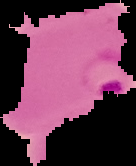
The area outside the segmented cell region is set to black. Image is 136×166 pixels. From a thin blood film. Result: malaria parasites detected.